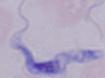

Summary:
  - Magnification: 1000x
  - Identification: trypanosome
  - Modality: micrograph